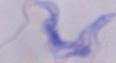
Summary:
  - Magnification: 1000x
  - Identification: trypanosome
  - Modality: micrograph